Identify the cell.
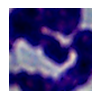
A leukocyte.

Captured at 1000x magnification. Photomicrograph.